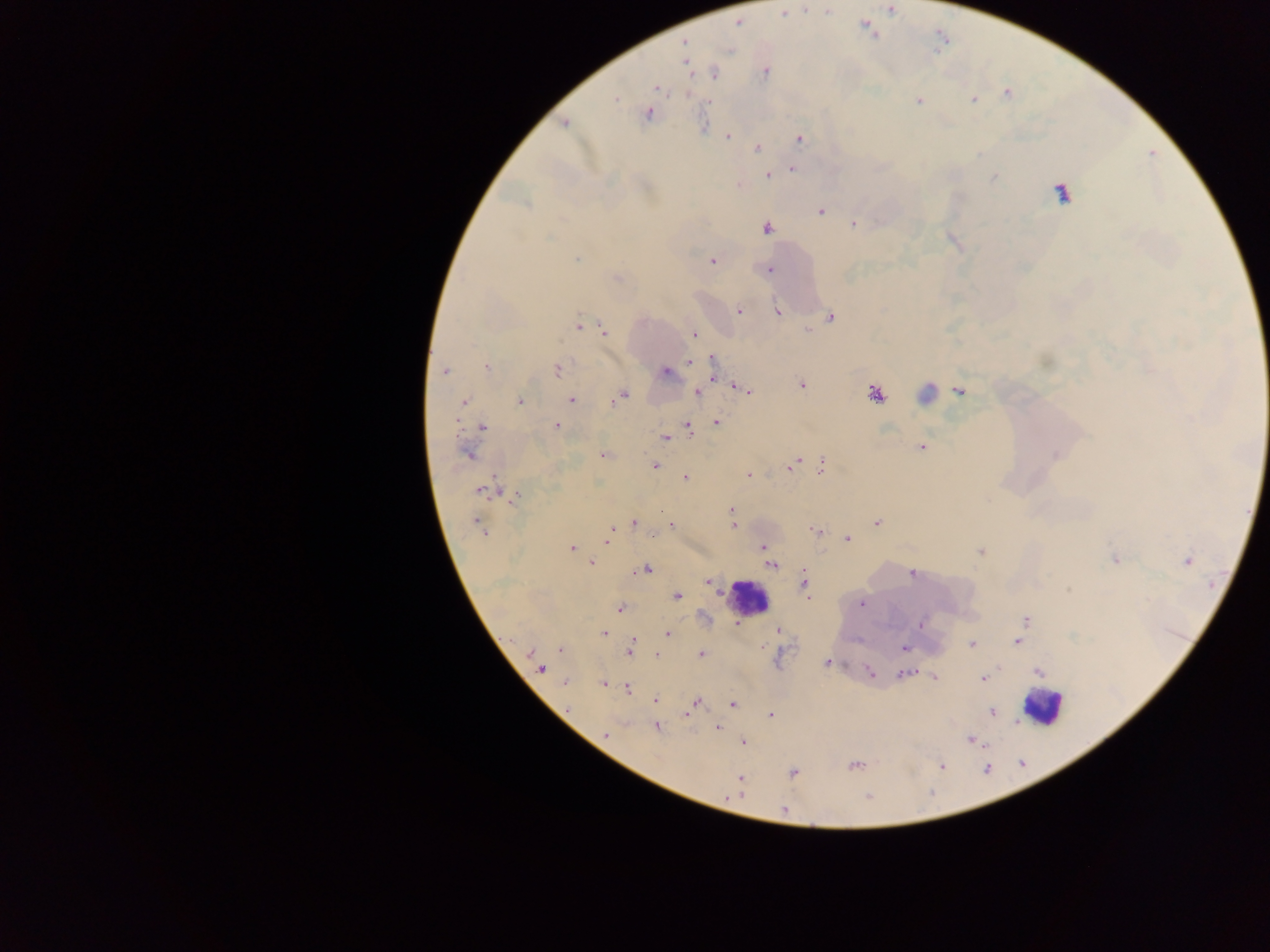
Approximate centers as [x, y] in pixels. Plasmodium parasite locations: [891, 9], [783, 12], [685, 42], [730, 50], [687, 65], [765, 73], [714, 74], [657, 88], [616, 99], [973, 99], [919, 101], [648, 114], [565, 123], [727, 136], [799, 138], [757, 149], [792, 168], [767, 176], [1061, 191], [820, 211], [854, 224], [766, 228], [576, 259], [712, 261], [769, 270], [617, 277], [739, 310], [778, 311], [831, 318], [578, 325], [604, 331], [694, 334], [713, 359], [689, 361], [485, 366], [557, 370], [445, 371], [666, 372], [802, 384], [735, 385], [743, 389], [959, 390], [698, 392], [874, 393], [622, 395], [572, 400], [616, 400], [519, 401], [463, 403], [716, 422], [556, 426], [482, 427], [689, 428], [666, 438], [921, 447], [467, 454], [602, 455], [797, 461], [655, 465], [792, 466], [821, 466], [748, 475], [685, 478], [482, 491], [514, 497], [731, 510], [634, 523], [876, 523], [477, 525], [671, 525], [733, 525], [612, 528], [814, 530], [608, 539], [847, 539], [572, 548], [764, 548], [981, 551], [1115, 559], [1187, 561], [591, 563], [772, 565], [646, 570], [911, 574], [709, 582], [804, 582], [678, 596], [862, 603], [619, 608], [1026, 619], [921, 624], [736, 625], [1022, 628], [779, 630], [604, 633], [668, 635], [1017, 642], [972, 644], [904, 648], [561, 650], [630, 650], [531, 653], [658, 654], [701, 654], [828, 662], [541, 670], [1039, 671], [871, 673], [903, 674], [933, 677], [982, 679], [565, 682], [604, 683], [627, 688], [655, 699], [695, 702], [733, 704], [688, 712], [992, 712], [770, 715], [657, 727], [717, 728], [606, 735], [971, 740], [743, 742], [854, 766], [942, 766], [793, 773], [740, 779], [784, 810]. Leukocyte locations: [925, 394], [748, 598], [1043, 708]. Thick blood smear. Image is 1270×952 pixels. Single field of view. Photographed through a microscope with a mobile-phone camera. Sample from Ghana.